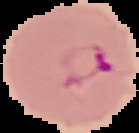
Summary:
  - Preparation: thin blood smear
  - Result: malaria parasites detected
  - Image type: segmented cell region with the area outside set to black
  - Image size: 139×133 pixels